Name the cell type shown.
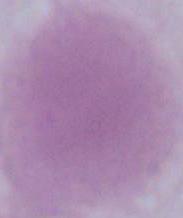
This is an erythrocyte.

Summary:
  - Magnification: 1000x
  - Modality: photomicrograph